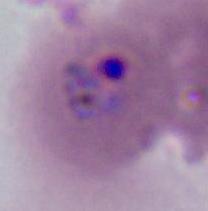
Summary:
  - Modality: photomicrograph
  - Identification: Plasmodium
  - Magnification: 400x or 1000x